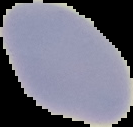

result = no Plasmodium parasites detected
image type = segmented cell region with the area outside set to black
image size = 133×127 pixels
preparation = thin blood film